Assess the morphology of the erythrocytes.
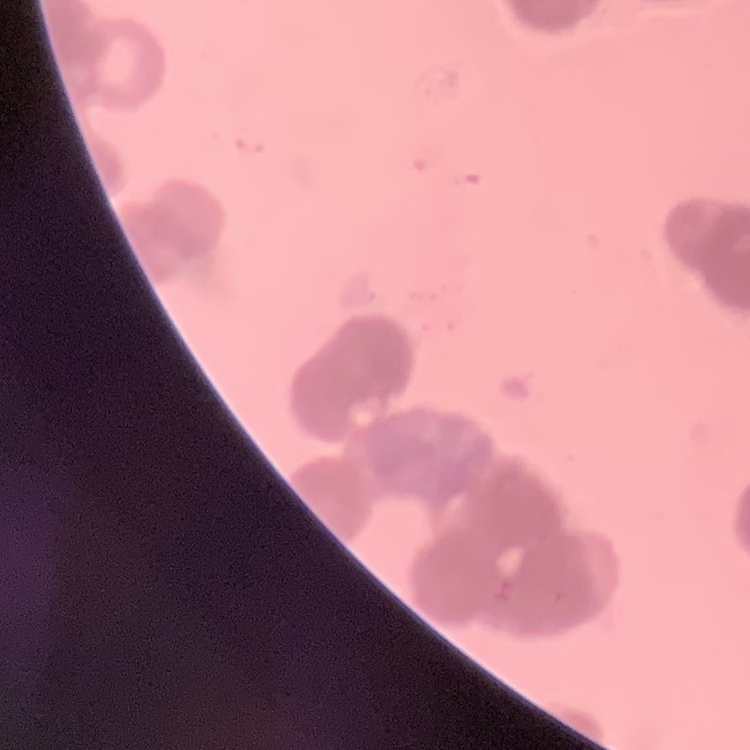
They show rouleaux formation.

Field's or Giemsa stain. Thin blood film. One tile cut from a larger photomicrograph.